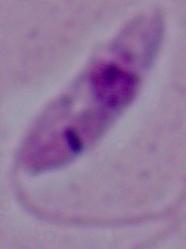
modality = micrograph
magnification = 1000x
identification = Leishmania